Comment on the morphology of the red blood cells.
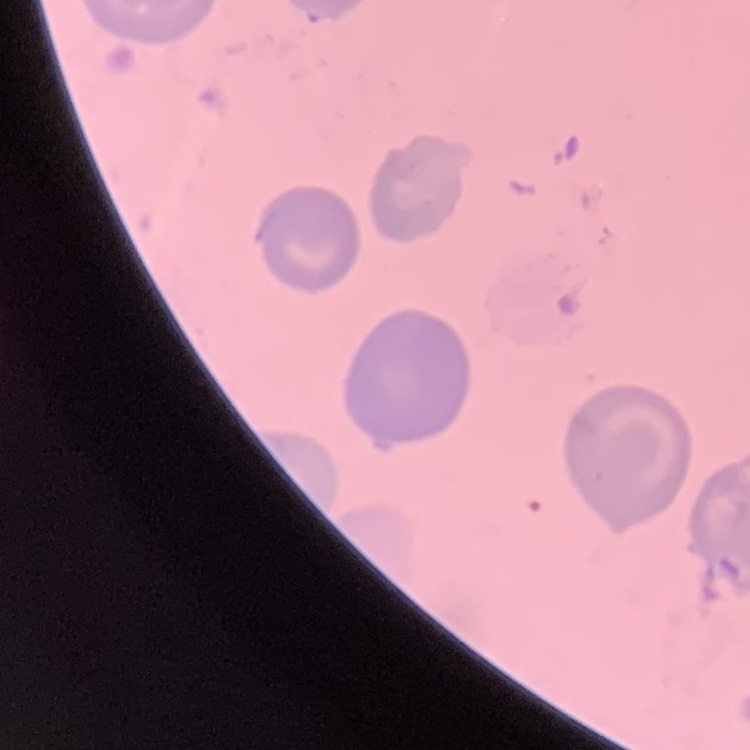

No rouleaux formation.

Stained with either Field's or Giemsa. One tile cut from a larger photomicrograph. Thin blood film.